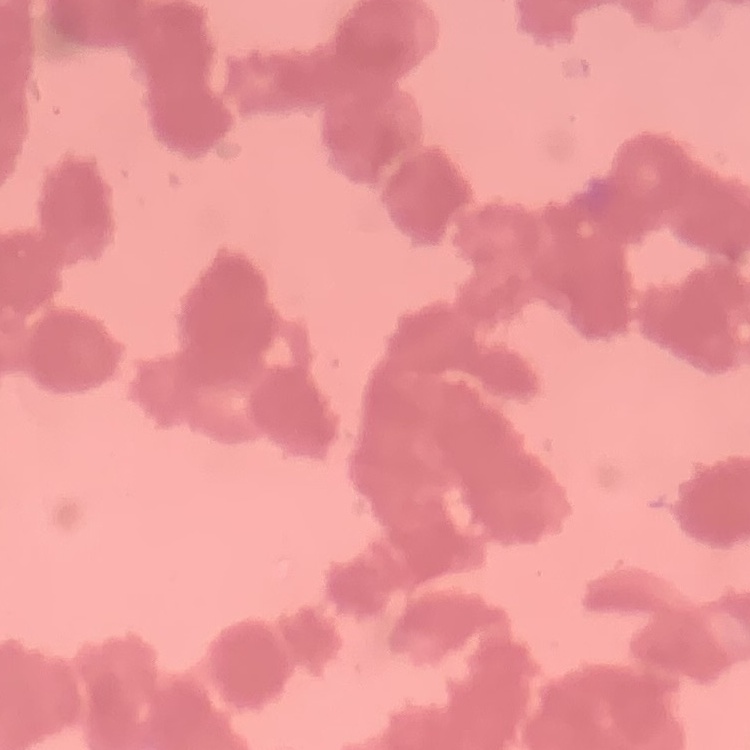

The red blood cells exhibit rouleaux formation. Thin peripheral smear. One tile cut from a larger photomicrograph. Field's or Giemsa stain.